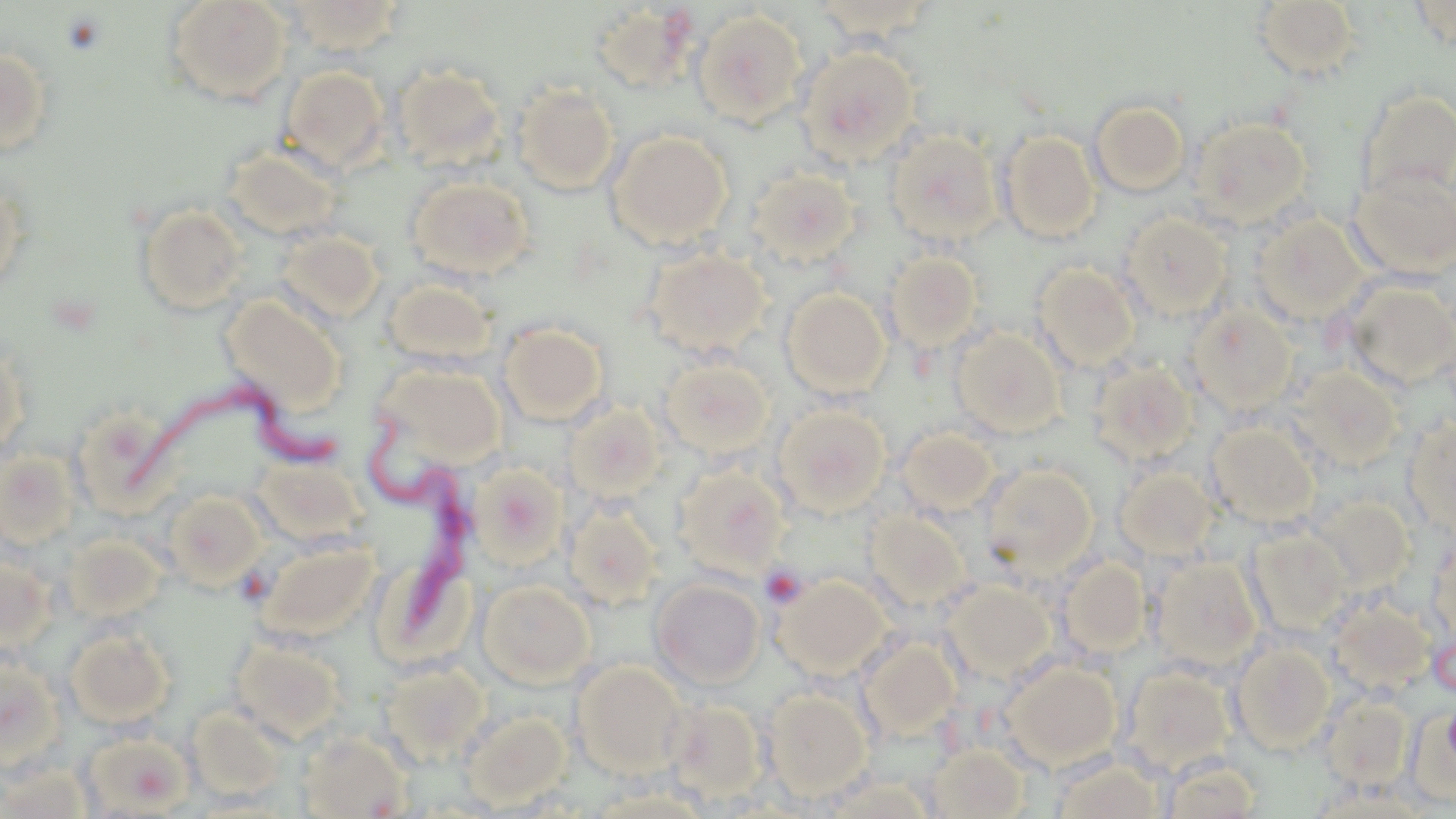
Summary:
  - Coordinate format: approximate bounding boxes as named x1/y1/x2/y2 corners in pixels
  - Trypanosoma brucei locations: (x1=125, y1=377, x2=338, y2=497), (x1=365, y1=412, x2=479, y2=651)
  - Platelet locations: (x1=759, y1=565, x2=807, y2=608)
  - Uninfected red blood cell locations: (x1=163, y1=0, x2=293, y2=105), (x1=282, y1=0, x2=406, y2=55), (x1=809, y1=1, x2=942, y2=45), (x1=1253, y1=1, x2=1362, y2=81), (x1=589, y1=3, x2=699, y2=93), (x1=692, y1=9, x2=809, y2=127), (x1=797, y1=45, x2=921, y2=165), (x1=0, y1=46, x2=55, y2=157), (x1=279, y1=65, x2=390, y2=173), (x1=394, y1=65, x2=506, y2=170), (x1=513, y1=82, x2=620, y2=195), (x1=1359, y1=89, x2=1456, y2=202), (x1=1089, y1=99, x2=1191, y2=197), (x1=1189, y1=116, x2=1313, y2=227), (x1=607, y1=129, x2=733, y2=248), (x1=885, y1=129, x2=1001, y2=246), (x1=998, y1=130, x2=1102, y2=243), (x1=223, y1=142, x2=345, y2=243), (x1=748, y1=167, x2=861, y2=265), (x1=1349, y1=167, x2=1456, y2=280), (x1=407, y1=175, x2=534, y2=281), (x1=0, y1=180, x2=28, y2=295), (x1=135, y1=203, x2=249, y2=316), (x1=1120, y1=213, x2=1232, y2=320), (x1=1250, y1=214, x2=1368, y2=324), (x1=277, y1=229, x2=385, y2=323), (x1=642, y1=246, x2=771, y2=358), (x1=885, y1=250, x2=984, y2=352), (x1=1033, y1=263, x2=1141, y2=371), (x1=382, y1=276, x2=498, y2=369), (x1=1343, y1=281, x2=1456, y2=390), (x1=781, y1=288, x2=890, y2=398), (x1=219, y1=294, x2=346, y2=414), (x1=1187, y1=306, x2=1297, y2=413), (x1=499, y1=322, x2=608, y2=427), (x1=951, y1=328, x2=1065, y2=437), (x1=0, y1=340, x2=29, y2=461), (x1=660, y1=356, x2=775, y2=460), (x1=1088, y1=359, x2=1199, y2=466), (x1=375, y1=362, x2=506, y2=466), (x1=1292, y1=365, x2=1404, y2=470), (x1=565, y1=401, x2=666, y2=501), (x1=773, y1=403, x2=891, y2=517), (x1=70, y1=408, x2=171, y2=516), (x1=1404, y1=416, x2=1456, y2=539), (x1=1206, y1=422, x2=1321, y2=528), (x1=897, y1=427, x2=1000, y2=516), (x1=0, y1=449, x2=79, y2=550), (x1=472, y1=464, x2=567, y2=567), (x1=673, y1=464, x2=789, y2=578), (x1=980, y1=464, x2=1097, y2=575), (x1=1115, y1=464, x2=1219, y2=561), (x1=164, y1=490, x2=267, y2=590), (x1=1310, y1=495, x2=1415, y2=594), (x1=565, y1=503, x2=662, y2=610), (x1=866, y1=510, x2=971, y2=612), (x1=1244, y1=527, x2=1351, y2=636), (x1=1428, y1=532, x2=1455, y2=648), (x1=63, y1=534, x2=167, y2=623), (x1=256, y1=537, x2=381, y2=641), (x1=0, y1=555, x2=56, y2=653), (x1=1149, y1=555, x2=1263, y2=673), (x1=1056, y1=557, x2=1150, y2=659), (x1=775, y1=574, x2=892, y2=680), (x1=651, y1=578, x2=765, y2=689), (x1=478, y1=579, x2=595, y2=688), (x1=943, y1=580, x2=1055, y2=683), (x1=1325, y1=595, x2=1435, y2=697), (x1=64, y1=625, x2=176, y2=727), (x1=228, y1=636, x2=346, y2=744), (x1=859, y1=637, x2=961, y2=740), (x1=1229, y1=640, x2=1336, y2=754), (x1=0, y1=656, x2=65, y2=769), (x1=379, y1=659, x2=490, y2=764), (x1=1003, y1=659, x2=1121, y2=768), (x1=571, y1=660, x2=688, y2=778), (x1=1120, y1=665, x2=1236, y2=777), (x1=764, y1=689, x2=871, y2=798), (x1=1320, y1=695, x2=1412, y2=790), (x1=662, y1=698, x2=767, y2=801), (x1=187, y1=707, x2=287, y2=804), (x1=462, y1=710, x2=570, y2=809), (x1=80, y1=730, x2=194, y2=816), (x1=296, y1=730, x2=413, y2=818), (x1=927, y1=743, x2=1030, y2=818), (x1=1159, y1=755, x2=1263, y2=818), (x1=1051, y1=757, x2=1164, y2=819), (x1=0, y1=764, x2=93, y2=818), (x1=825, y1=775, x2=933, y2=817)
  - Slide-level diagnosis: Trypanosoma brucei
  - Field of view: single
  - Stain: May-Grünwald-Giemsa
  - Modality: light microscopy
  - Magnification: 1000x
  - Image size: 1456×819 pixels
  - Preparation: thin blood smear